Point out each Plasmodium parasite.
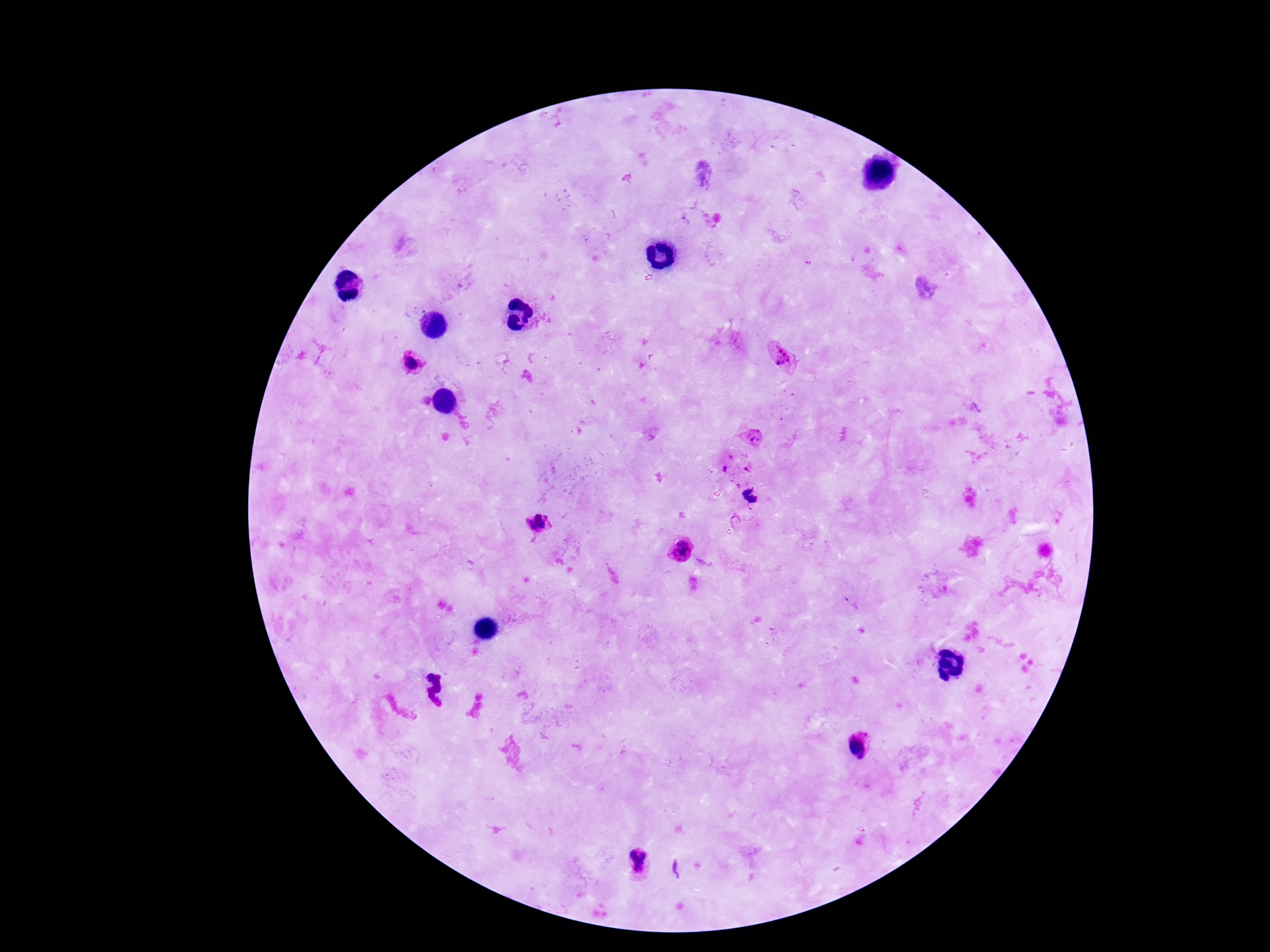
Approximate centers as [x, y] in pixels.
Plasmodium parasites: [781, 358], [412, 363], [753, 439], [730, 457], [724, 469], [747, 469], [537, 522], [534, 540], [680, 551], [857, 748], [639, 862].

{
  "image_size": "1270×952 pixels",
  "capture": "smartphone camera through the microscope eyepiece",
  "preparation": "thick blood smear",
  "magnification": "100x",
  "field_of_view": "one from this slide",
  "patient_malaria_status": "positive",
  "stain": "Giemsa"
}